Assess this cell for malaria.
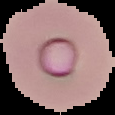
It is parasitized.

Image is 115×115 pixels. From a thin blood smear. Cell region segmented out of the field of view; the surrounding area is masked to black.